Describe the morphology of the erythrocytes.
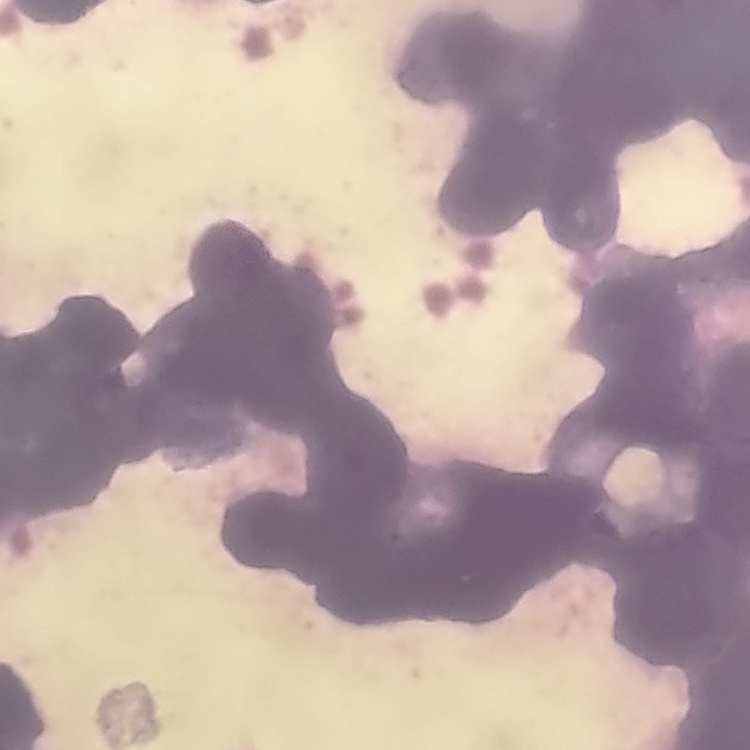
They show rouleaux formation.

Stained with either Field's or Giemsa. Thin peripheral smear. Square crop of a larger photomicrograph.